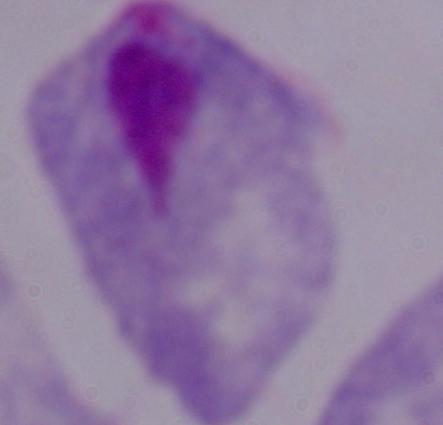 A trichomonad is seen. Micrograph. 1000x magnification.